Describe the morphology of the erythrocytes.
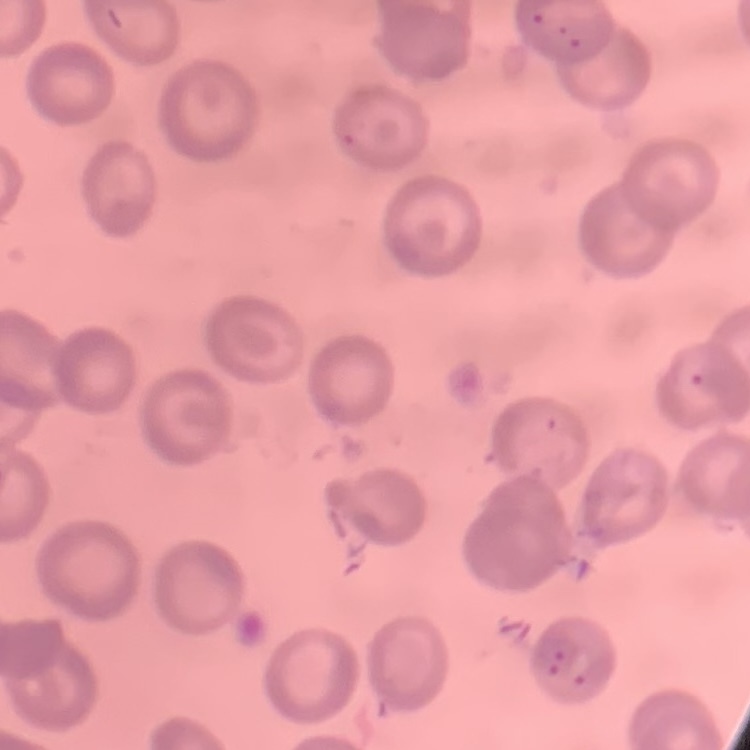
They show no rouleaux formation.

Summary:
  - Image type: one tile cut from a larger photomicrograph
  - Preparation: thin blood smear
  - Stain: Field's or Giemsa